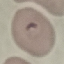
Malaria status: parasitized. Giemsa-stained preparation. Thin smear of blood. Cell patch, automatically extracted from a larger field of view and resized to 64 × 64 pixels. Acquired by smartphone through the microscope eyepiece.